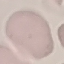
Summary:
  - Result: no malaria parasites seen
  - Stain: Giemsa
  - Image type: automatically extracted cell patch, resized to 64 × 64 pixels
  - Capture: smartphone camera at the microscope eyepiece
  - Preparation: thin blood smear